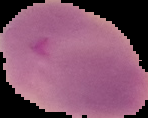

Summary:
  - Image type: cell region segmented out of the field of view; surrounding area masked to black
  - Preparation: thin blood smear
  - Malaria status: uninfected
  - Image size: 148×118 pixels